Classify this cell by malaria status.
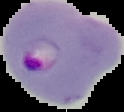

Parasitized.

Cell region segmented out of the field of view; the surrounding area is masked to black. Image is 124×112 pixels. From a thin blood smear.